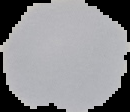

Summary:
  - Image size: 130×112 pixels
  - Preparation: thin blood smear
  - Image type: cell region segmented out of the field of view; surrounding area masked to black
  - Result: no malaria parasites detected